Classify this cell by malaria status.
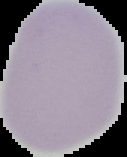
Uninfected.

preparation = thin blood film
image size = 127×157 pixels
image type = cell region segmented out of the field of view; surrounding area masked to black